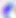

Summary:
  - Magnification: 400x
  - Identification: Toxoplasma gondii
  - Modality: micrograph